Report the malaria status of this cell.
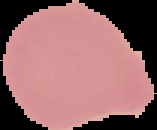

Uninfected.

Summary:
  - Image size: 157×130 pixels
  - Preparation: thin blood film
  - Image type: segmented cell region with the area outside set to black